Describe the morphology of the erythrocytes.
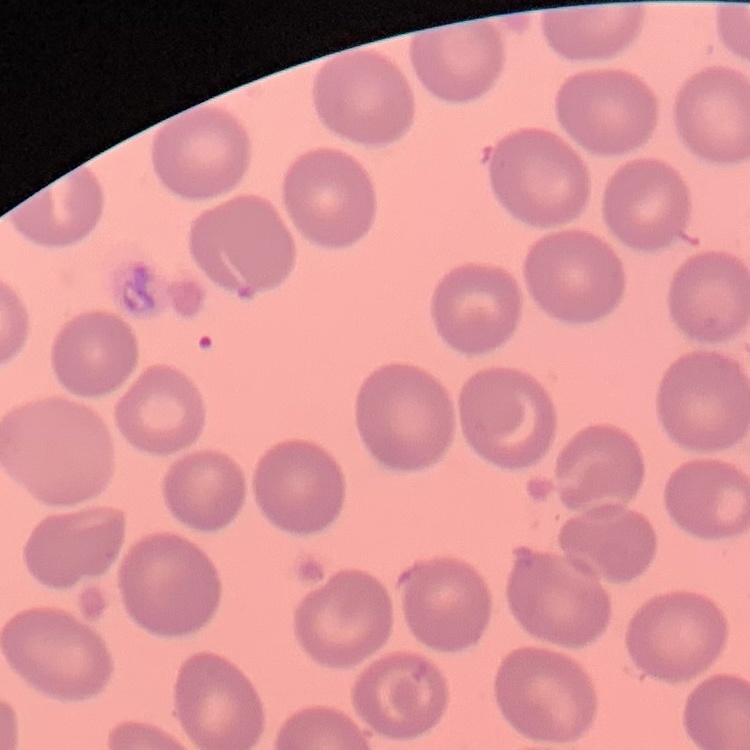

They show no rouleaux formation.

Square crop of a larger photomicrograph. Thin blood smear. Stained with either Field's or Giemsa.